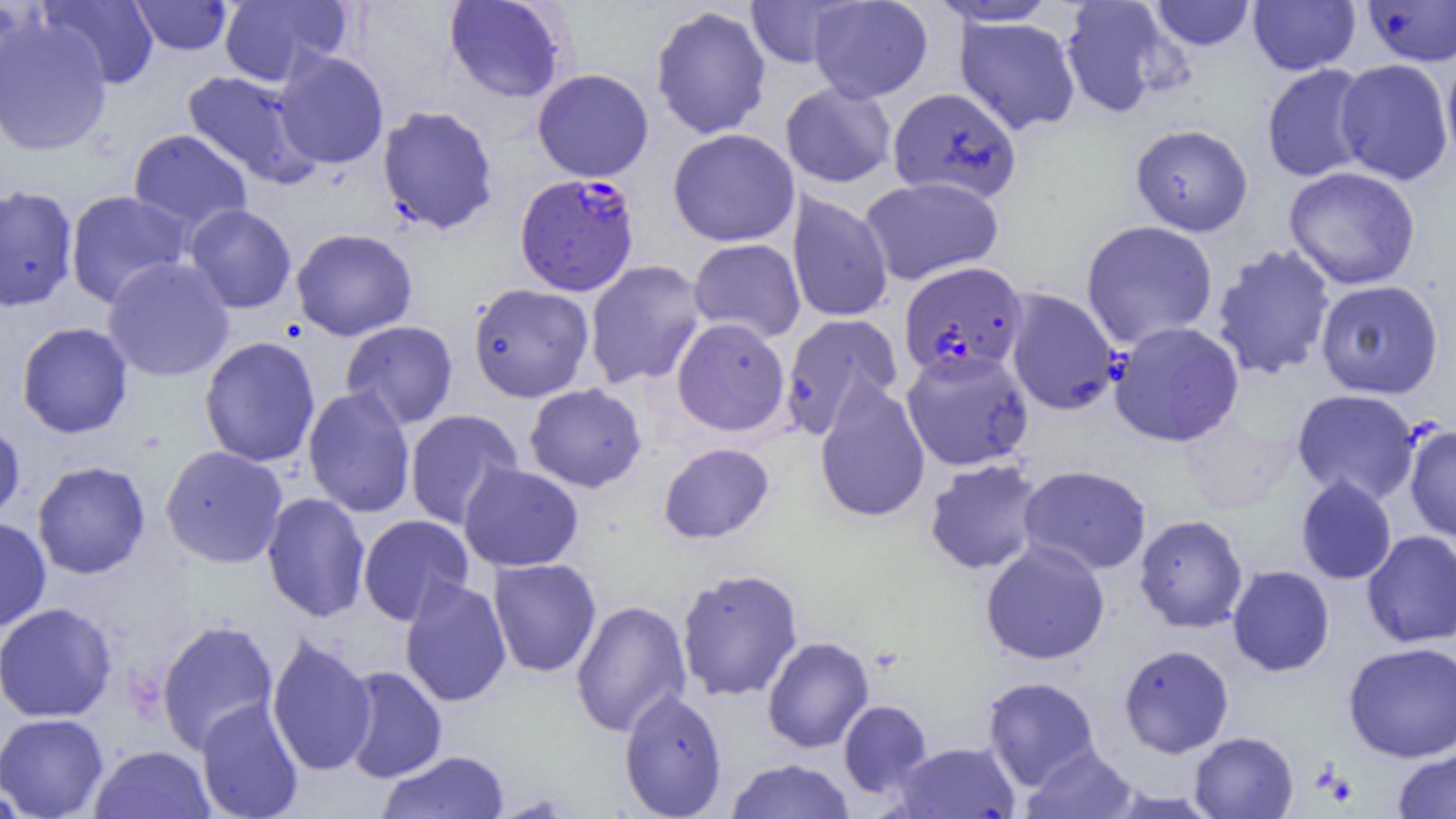

Summary:
  - Coordinate format: approximate bounding boxes as (x1,y1)-(x2,y2) corner pairs in pixels
  - Uninfected red blood cell locations: (0,0)-(36,106), (39,0)-(159,89), (219,0)-(351,86), (807,0)-(933,102), (1151,0)-(1256,51), (130,1)-(232,54), (443,1)-(570,103), (745,1)-(855,69), (928,1)-(1062,27), (1059,1)-(1179,118), (1248,1)-(1361,75), (1361,1)-(1456,66), (651,5)-(772,139), (0,15)-(112,157), (954,16)-(1081,135), (274,50)-(389,169), (1442,54)-(1456,170), (1335,58)-(1453,185), (1261,63)-(1374,183), (532,68)-(654,182), (181,70)-(317,186), (780,81)-(897,188), (888,87)-(1022,203), (377,105)-(499,235), (1130,123)-(1253,236), (127,128)-(252,235), (668,128)-(799,247), (1284,166)-(1421,290), (859,176)-(1003,285), (0,184)-(79,312), (64,190)-(193,308), (787,191)-(893,323), (184,204)-(296,313), (1081,220)-(1218,348), (290,228)-(418,341), (688,238)-(805,343), (1211,244)-(1336,381), (101,256)-(235,383), (584,260)-(707,389), (1315,280)-(1444,399), (467,282)-(594,402), (1004,288)-(1120,416), (779,315)-(902,440), (671,317)-(790,436), (340,320)-(458,429), (16,321)-(133,439), (1109,321)-(1244,447), (199,336)-(321,468), (901,349)-(1034,471), (814,376)-(930,523), (524,383)-(647,493), (302,386)-(416,518), (1291,389)-(1421,505), (404,409)-(523,530), (1178,415)-(1297,514), (0,419)-(26,528), (1405,424)-(1456,542), (658,442)-(774,544), (159,445)-(288,568), (924,458)-(1045,575), (32,460)-(151,579), (459,462)-(584,572), (1018,465)-(1152,575), (1295,475)-(1398,585), (261,492)-(370,623), (358,514)-(475,625), (1134,514)-(1249,633), (0,517)-(51,631), (1361,530)-(1456,648), (980,540)-(1110,665), (488,558)-(601,677), (1227,565)-(1335,676), (676,567)-(804,702), (400,577)-(511,708), (570,599)-(691,737), (0,602)-(118,722), (155,618)-(280,754), (266,633)-(376,776), (762,636)-(874,753), (1343,641)-(1456,763), (1118,644)-(1234,757), (340,666)-(447,783), (982,676)-(1101,790), (619,687)-(727,818), (196,698)-(304,819), (838,700)-(933,799), (0,713)-(109,819), (1189,731)-(1298,818), (894,741)-(1020,819), (89,744)-(215,818), (1022,745)-(1138,819), (1391,746)-(1456,818), (376,750)-(509,819), (725,758)-(856,818), (0,781)-(32,819)
  - Plasmodium falciparum-infected red blood cell locations: (515,172)-(640,295), (898,262)-(1028,383)
  - Slide-level diagnosis: Plasmodium falciparum
  - Field of view: one of a larger specimen
  - Image size: 1456×819 pixels
  - Preparation: thin blood film
  - Modality: light microscopy
  - Magnification: 1000x